Locate every blood parasite and identify its species.
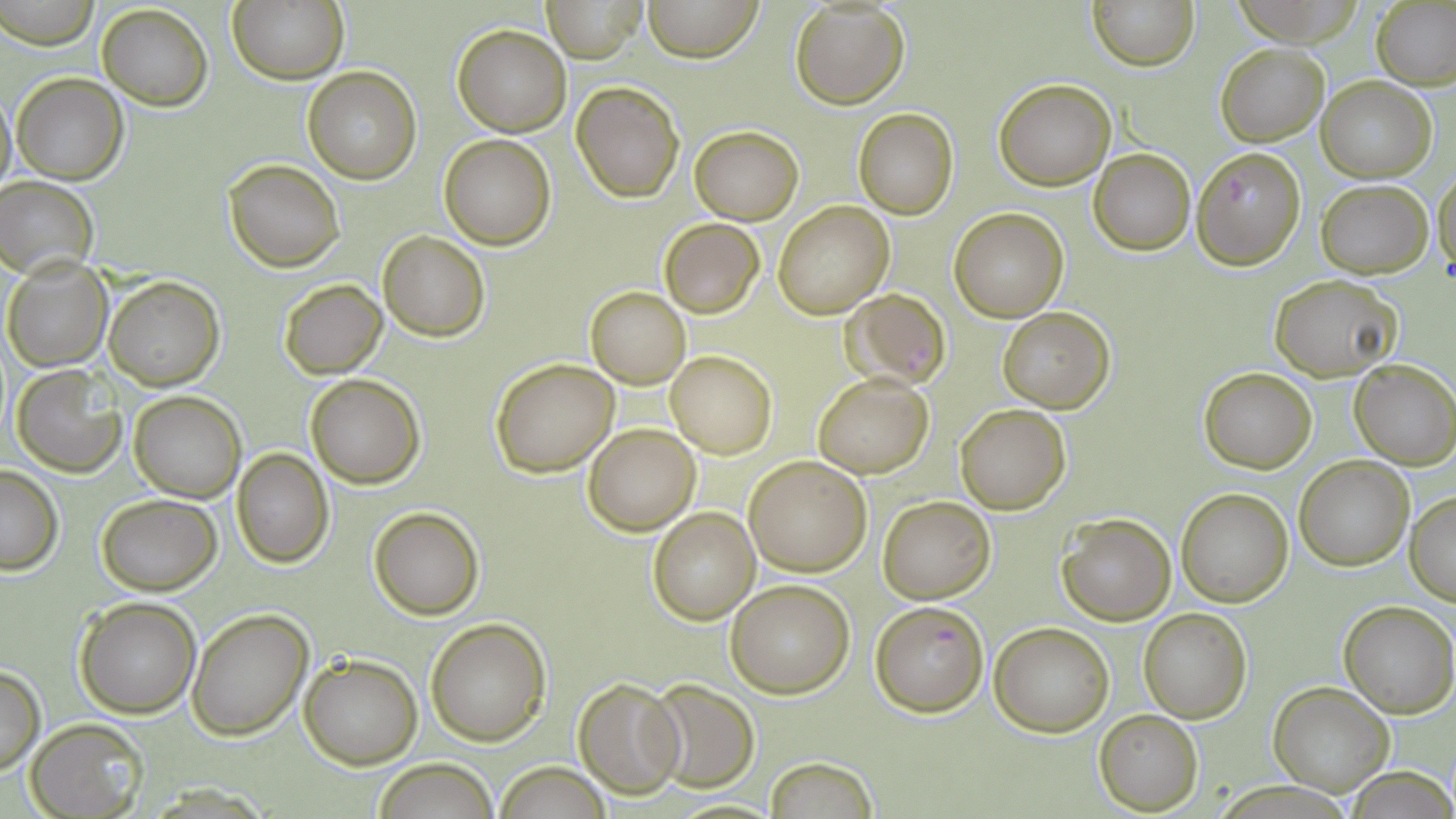
Approximate bounding boxes as named x1/y1/x2/y2 corners in pixels.
Plasmodium falciparum-infected red blood cells: (x1=1189, y1=145, x2=1306, y2=268), (x1=844, y1=289, x2=951, y2=391), (x1=871, y1=599, x2=989, y2=715).
No Plasmodium ovale, Plasmodium malariae, Plasmodium vivax, Babesia divergens, or Trypanosoma brucei observed.

slide_level_diagnosis: Plasmodium falciparum
preparation: thin blood film
field_of_view: single
stain: May-Grünwald-Giemsa
modality: light microscopy
image_size: 1456×819 pixels
magnification: 1000x
uninfected_red_blood_cell_locations: 'approximate bounding boxes as named x1/y1/x2/y2 corners in pixels: (x1=228, y1=0, x2=347, y2=85), (x1=541, y1=0, x2=647, y2=62), (x1=641, y1=0, x2=763, y2=64), (x1=1087, y1=0, x2=1199, y2=71), (x1=2, y1=2, x2=99, y2=49), (x1=1373, y1=2, x2=1456, y2=90), (x1=96, y1=3, x2=214, y2=111), (x1=788, y1=3, x2=911, y2=110), (x1=452, y1=24, x2=571, y2=135), (x1=1216, y1=42, x2=1328, y2=146), (x1=302, y1=66, x2=421, y2=184), (x1=11, y1=72, x2=127, y2=184), (x1=1317, y1=77, x2=1436, y2=181), (x1=993, y1=78, x2=1116, y2=190), (x1=571, y1=81, x2=683, y2=202), (x1=0, y1=83, x2=16, y2=197), (x1=853, y1=107, x2=959, y2=219), (x1=690, y1=126, x2=803, y2=224), (x1=440, y1=134, x2=556, y2=250), (x1=1088, y1=147, x2=1195, y2=256), (x1=223, y1=158, x2=346, y2=272), (x1=1432, y1=166, x2=1455, y2=282), (x1=0, y1=178, x2=99, y2=278), (x1=1316, y1=180, x2=1433, y2=277), (x1=772, y1=201, x2=893, y2=319), (x1=950, y1=208, x2=1068, y2=323), (x1=659, y1=218, x2=763, y2=317), (x1=378, y1=231, x2=489, y2=342), (x1=2, y1=257, x2=114, y2=372), (x1=1270, y1=275, x2=1401, y2=380), (x1=105, y1=276, x2=224, y2=389), (x1=279, y1=280, x2=387, y2=378), (x1=585, y1=287, x2=690, y2=388), (x1=997, y1=306, x2=1116, y2=412), (x1=666, y1=352, x2=776, y2=458), (x1=491, y1=357, x2=619, y2=476), (x1=1350, y1=359, x2=1456, y2=469), (x1=10, y1=364, x2=128, y2=478), (x1=1198, y1=366, x2=1318, y2=474), (x1=812, y1=373, x2=934, y2=479), (x1=307, y1=374, x2=424, y2=489), (x1=128, y1=390, x2=247, y2=502), (x1=954, y1=404, x2=1071, y2=514), (x1=583, y1=424, x2=700, y2=536), (x1=232, y1=448, x2=334, y2=568), (x1=743, y1=456, x2=873, y2=575), (x1=1294, y1=457, x2=1413, y2=570), (x1=0, y1=465, x2=63, y2=575), (x1=1175, y1=489, x2=1293, y2=607), (x1=1406, y1=491, x2=1456, y2=605), (x1=97, y1=493, x2=220, y2=595), (x1=878, y1=496, x2=995, y2=603), (x1=369, y1=505, x2=485, y2=621), (x1=646, y1=507, x2=760, y2=625), (x1=1057, y1=512, x2=1174, y2=625), (x1=726, y1=580, x2=854, y2=698), (x1=74, y1=597, x2=202, y2=718), (x1=1339, y1=601, x2=1456, y2=718), (x1=187, y1=607, x2=312, y2=741), (x1=1137, y1=608, x2=1252, y2=724), (x1=425, y1=618, x2=551, y2=746), (x1=989, y1=622, x2=1114, y2=736), (x1=298, y1=653, x2=422, y2=769), (x1=0, y1=666, x2=45, y2=775), (x1=572, y1=676, x2=685, y2=800), (x1=645, y1=679, x2=760, y2=791), (x1=1267, y1=681, x2=1395, y2=797), (x1=1095, y1=710, x2=1203, y2=814), (x1=26, y1=717, x2=147, y2=819), (x1=765, y1=755, x2=880, y2=819), (x1=372, y1=758, x2=499, y2=818), (x1=493, y1=763, x2=614, y2=818), (x1=1345, y1=768, x2=1456, y2=818)'